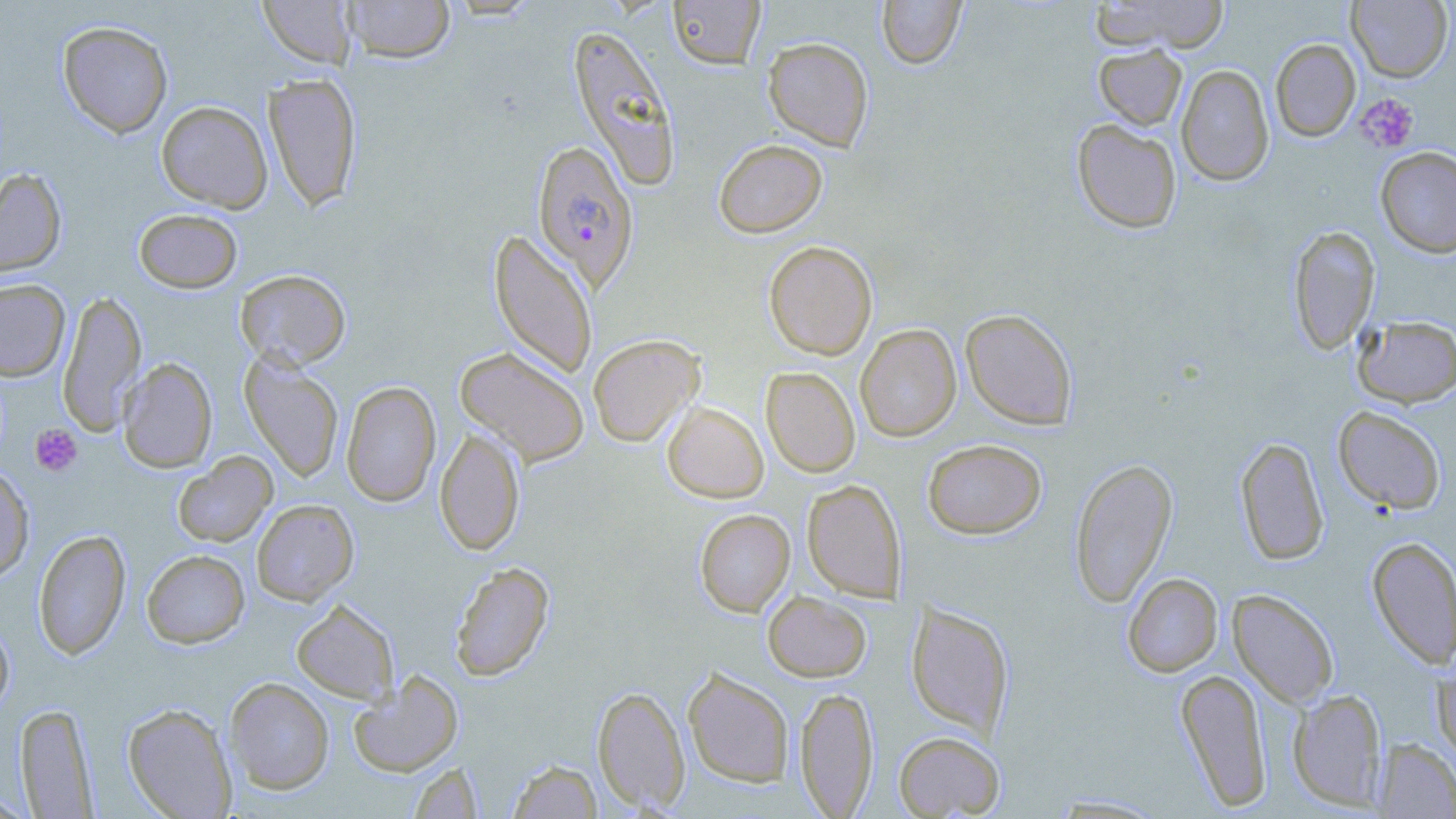

Approximate bounding boxes as named x1/y1/x2/y2 corners in pixels. Platelet locations: (x1=1356, y1=94, x2=1419, y2=153), (x1=30, y1=423, x2=83, y2=476). Uninfected red blood cell locations: (x1=340, y1=0, x2=456, y2=63), (x1=668, y1=0, x2=766, y2=69), (x1=876, y1=0, x2=966, y2=68), (x1=1090, y1=0, x2=1230, y2=54), (x1=1347, y1=0, x2=1453, y2=82), (x1=258, y1=1, x2=357, y2=69), (x1=57, y1=20, x2=173, y2=138), (x1=567, y1=24, x2=682, y2=190), (x1=762, y1=37, x2=874, y2=151), (x1=1270, y1=38, x2=1361, y2=141), (x1=1094, y1=44, x2=1187, y2=130), (x1=1176, y1=63, x2=1274, y2=186), (x1=264, y1=72, x2=362, y2=211), (x1=156, y1=101, x2=273, y2=212), (x1=1072, y1=119, x2=1182, y2=233), (x1=713, y1=139, x2=827, y2=238), (x1=1375, y1=146, x2=1456, y2=258), (x1=0, y1=167, x2=67, y2=278), (x1=133, y1=208, x2=242, y2=293), (x1=1288, y1=225, x2=1380, y2=354), (x1=489, y1=229, x2=598, y2=380), (x1=764, y1=240, x2=878, y2=360), (x1=235, y1=269, x2=351, y2=370), (x1=0, y1=278, x2=70, y2=381), (x1=57, y1=289, x2=146, y2=435), (x1=960, y1=308, x2=1078, y2=430), (x1=1354, y1=315, x2=1456, y2=407), (x1=855, y1=323, x2=961, y2=441), (x1=588, y1=334, x2=704, y2=447), (x1=455, y1=346, x2=590, y2=466), (x1=240, y1=354, x2=344, y2=482), (x1=117, y1=358, x2=217, y2=472), (x1=761, y1=367, x2=860, y2=477), (x1=341, y1=381, x2=441, y2=507), (x1=662, y1=402, x2=768, y2=503), (x1=1333, y1=405, x2=1447, y2=514), (x1=435, y1=426, x2=525, y2=556), (x1=1235, y1=437, x2=1329, y2=566), (x1=923, y1=438, x2=1047, y2=539), (x1=173, y1=452, x2=277, y2=547), (x1=1069, y1=457, x2=1177, y2=607), (x1=0, y1=464, x2=35, y2=582), (x1=802, y1=479, x2=907, y2=601), (x1=251, y1=499, x2=359, y2=605), (x1=694, y1=509, x2=795, y2=616), (x1=33, y1=529, x2=131, y2=660), (x1=1367, y1=536, x2=1456, y2=669), (x1=142, y1=550, x2=250, y2=648), (x1=449, y1=561, x2=554, y2=682), (x1=1123, y1=573, x2=1223, y2=676), (x1=1228, y1=589, x2=1339, y2=708), (x1=763, y1=591, x2=871, y2=681), (x1=291, y1=599, x2=399, y2=703), (x1=906, y1=600, x2=1014, y2=739), (x1=0, y1=618, x2=15, y2=717), (x1=1432, y1=662, x2=1456, y2=764), (x1=683, y1=667, x2=794, y2=788), (x1=1175, y1=668, x2=1272, y2=811), (x1=347, y1=671, x2=464, y2=777), (x1=224, y1=677, x2=334, y2=794), (x1=592, y1=685, x2=691, y2=813), (x1=795, y1=686, x2=878, y2=816), (x1=1288, y1=688, x2=1387, y2=809), (x1=14, y1=703, x2=97, y2=818), (x1=123, y1=703, x2=238, y2=818), (x1=893, y1=730, x2=1005, y2=818), (x1=1373, y1=738, x2=1456, y2=818), (x1=507, y1=759, x2=602, y2=818), (x1=408, y1=762, x2=483, y2=819), (x1=0, y1=792, x2=38, y2=819), (x1=1044, y1=794, x2=1173, y2=818). Plasmodium falciparum-infected red blood cell locations: (x1=532, y1=139, x2=639, y2=290). Slide-level diagnosis: Plasmodium falciparum. Captured at 1000x magnification. Single field of view. Optical microscopy. Thin blood smear. Image is 1456×819 pixels. May-Grünwald-Giemsa stain.